Report the malaria status of this cell.
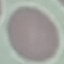

It is uninfected.

Cell patch, automatically extracted from a larger field of view and resized to 64 × 64 pixels. Thin smear of blood. Giemsa stain. Photographed with a smartphone camera at the microscope eyepiece.